Evaluate for Plasmodium parasites.
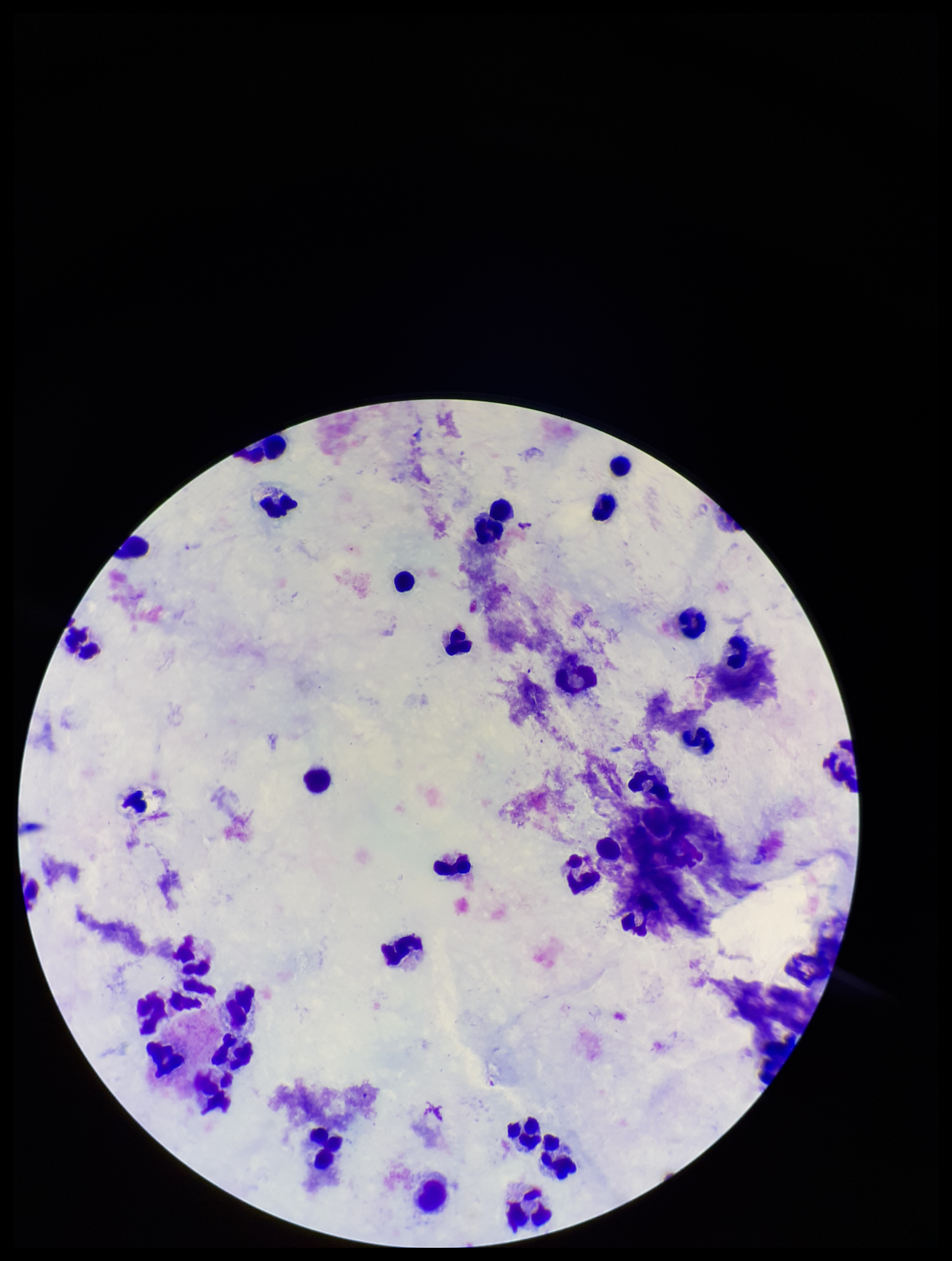

None detected.

{
  "parasite_count": 0,
  "image_size": "952×1261 pixels",
  "patient_malaria_status": "negative",
  "leukocyte_count": 36,
  "preparation": "thick",
  "capture": "smartphone photograph through the microscope eyepiece",
  "field_of_view": "single",
  "stain": "Giemsa"
}